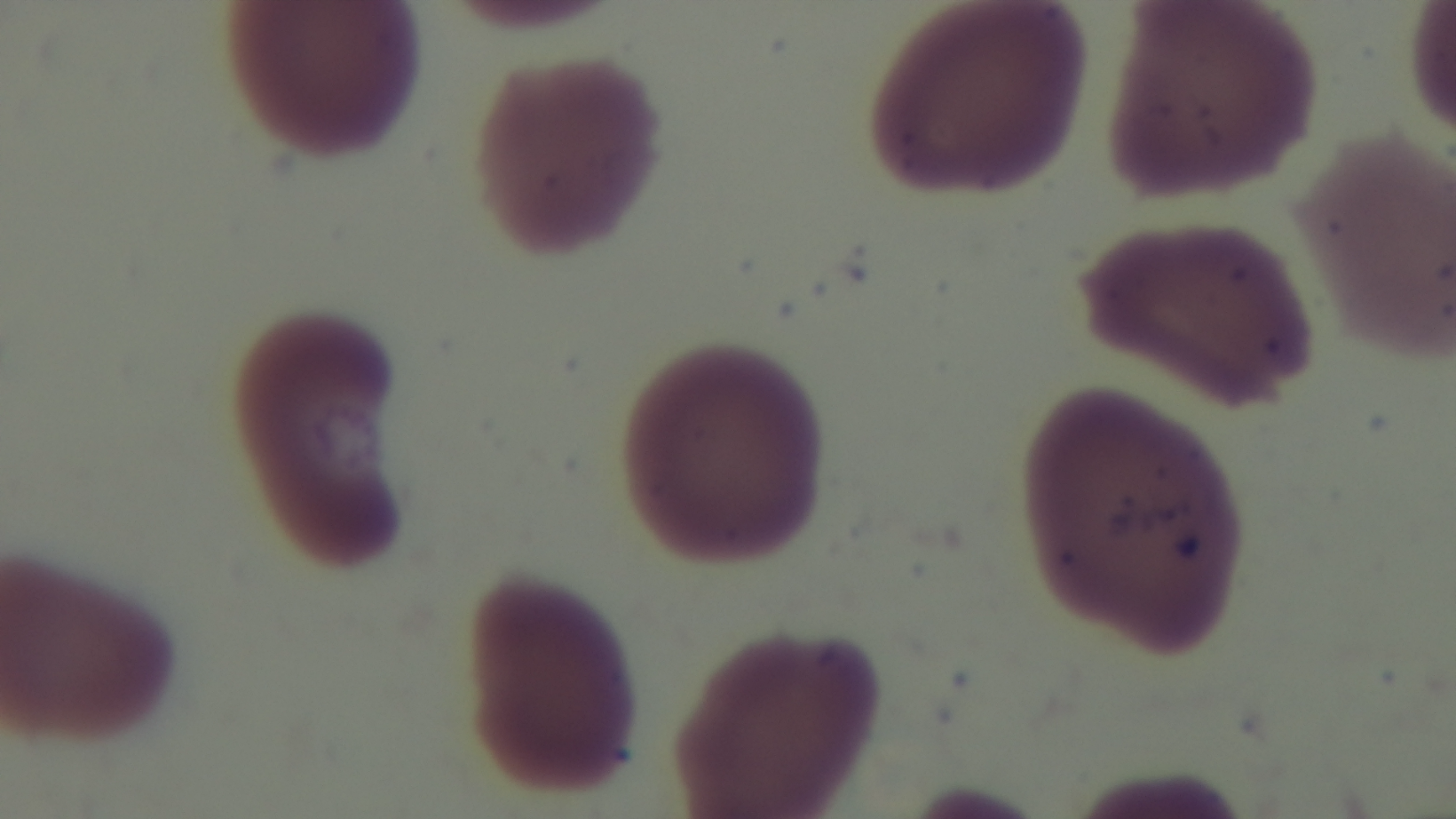

Giemsa-stained. Mounted 4K digital camera. Malaria status: negative. Light microscopy. One field from the slide. Preparation: thin. Oil-immersion objective, 100x.